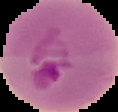
{
  "image_size": "118×112 pixels",
  "image_type": "segmented cell region on a black background",
  "result": "malaria parasites identified",
  "preparation": "thin blood smear"
}